Classify this cell by malaria status.
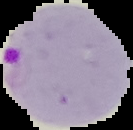
Parasitized.

{
  "preparation": "thin blood smear",
  "image_type": "cell region segmented out of the field of view; surrounding area masked to black",
  "image_size": "133×130 pixels"
}